Assess the morphology of the red blood cells.
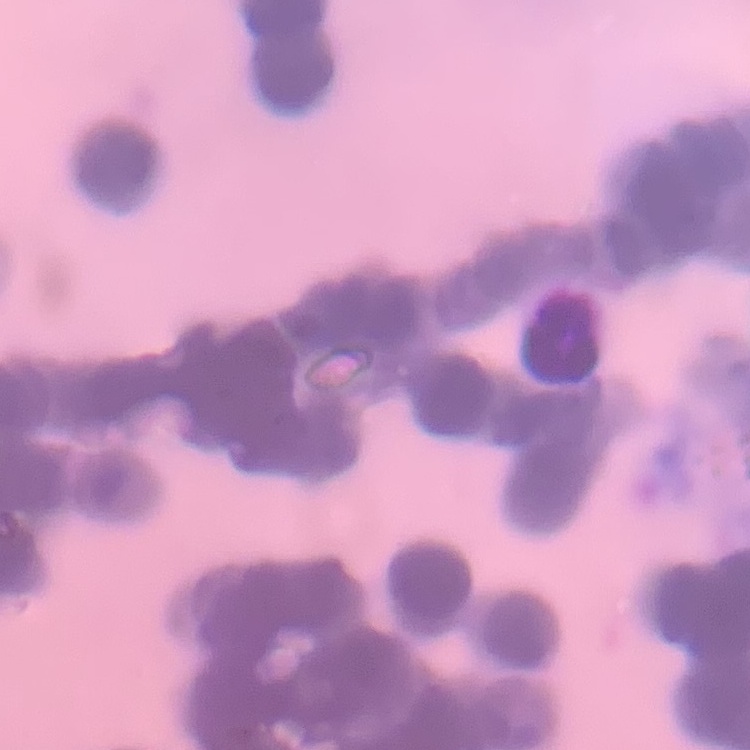

They show rouleaux formation.

stain = Field's or Giemsa
preparation = thin blood film
image type = square crop of a larger photomicrograph